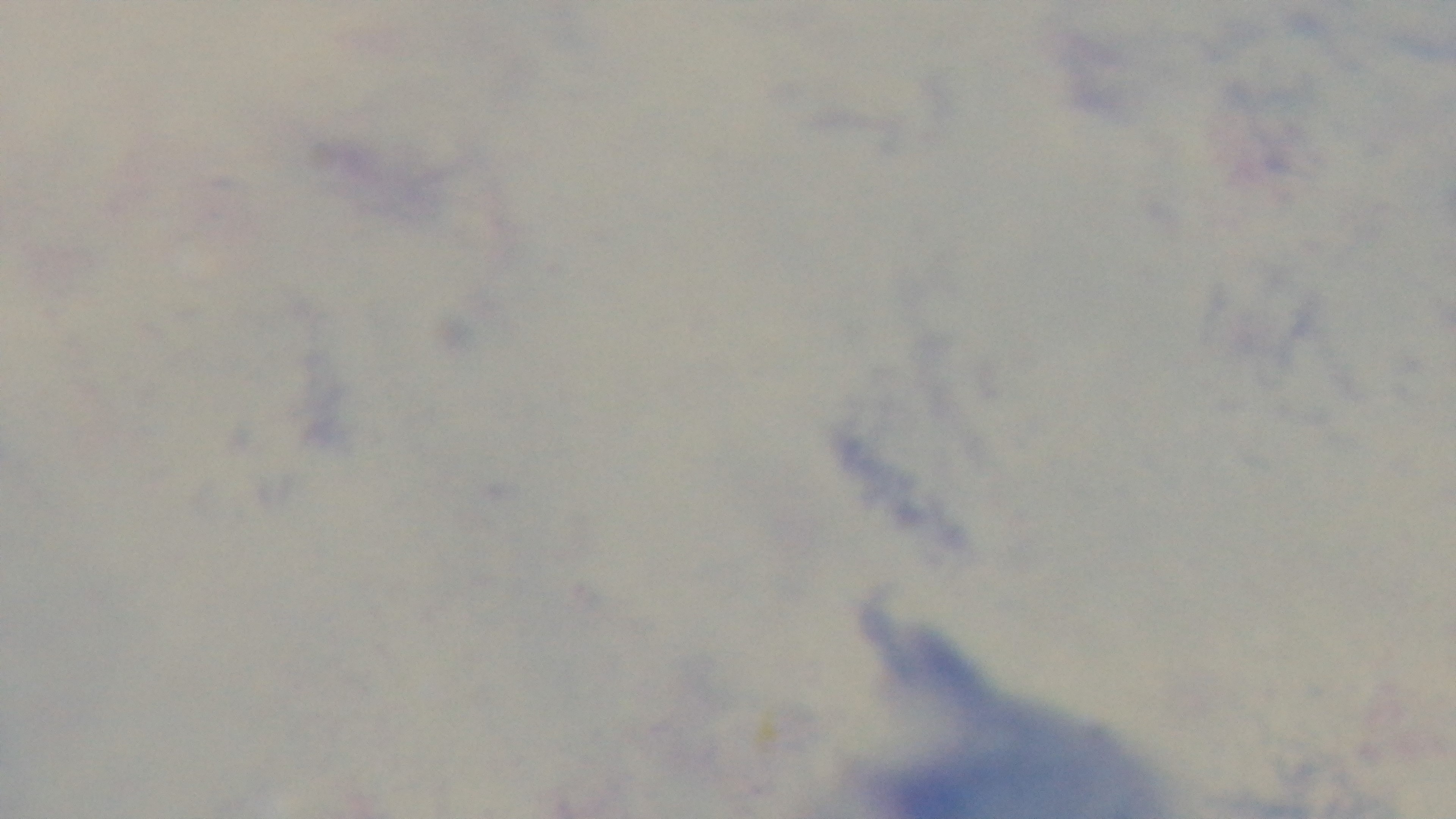
field_of_view: single
modality: light microscopy
objective: 100x oil immersion
capture: mounted 4K digital camera
stain: Giemsa
preparation: thick smear
malaria_status: uninfected